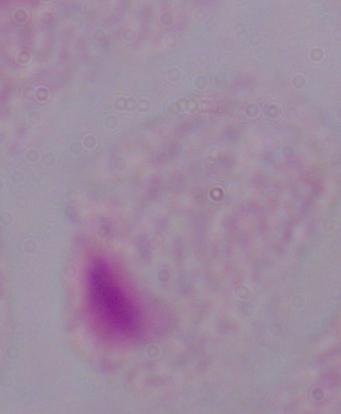
Captured at 1000x magnification. Micrograph. A trichomonad is seen.